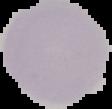

Malaria status: uninfected. From a thin blood smear. Image is 112×109 pixels. The area outside the segmented cell region is set to black.